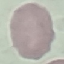

Summary:
  - Malaria status: uninfected
  - Preparation: thin blood smear
  - Capture: smartphone camera at the microscope eyepiece
  - Stain: Giemsa
  - Image type: automatically extracted cell patch, resized to 64 × 64 pixels